Report the malaria status of this cell.
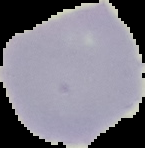

Uninfected.

Image is 145×148 pixels. From a thin blood smear. Cell region segmented out of the field of view; the surrounding area is masked to black.